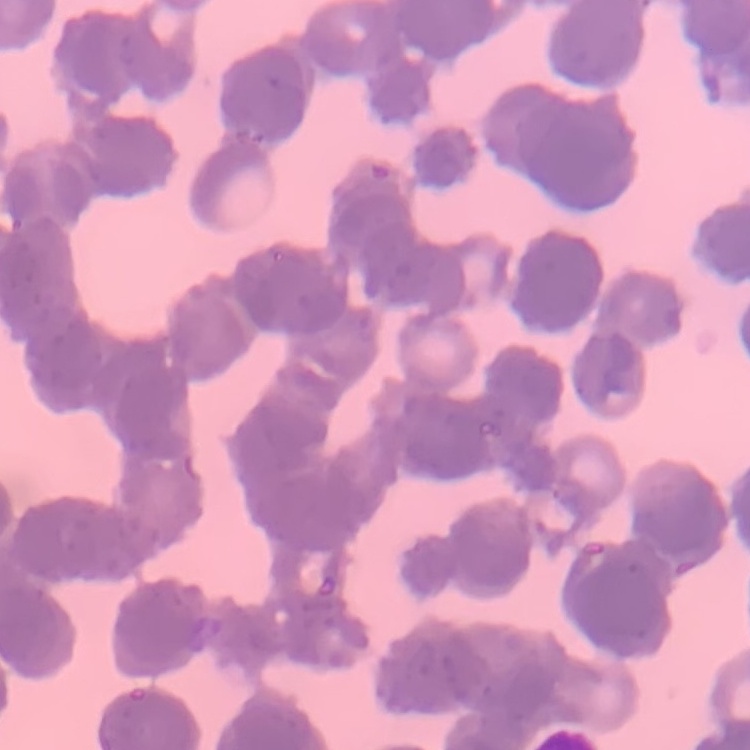
The red blood cells exhibit rouleaux formation. Field's or Giemsa stain. One tile cut from a larger photomicrograph. Thin blood film.